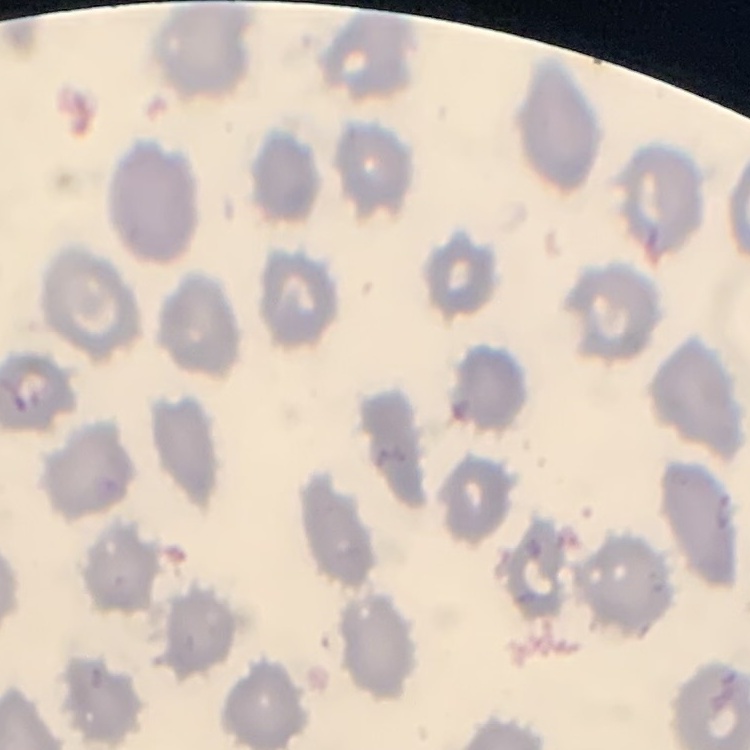
The red blood cells show no rouleaux formation. Thin blood smear. Field's or Giemsa stain. One tile cut from a larger photomicrograph.